Report the malaria status of this cell.
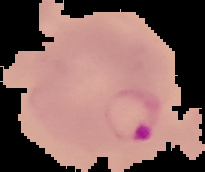

It is parasitized.

image size = 205×172 pixels
image type = segmented cell region with the area outside set to black
preparation = thin blood smear